Assess the morphology of the erythrocytes.
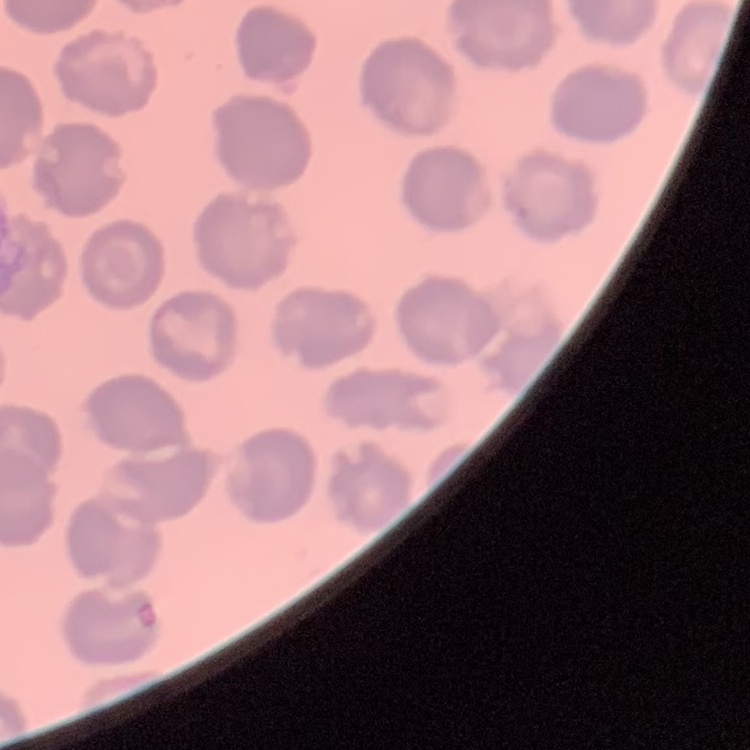
No rouleaux formation.

Summary:
  - Image type: one tile cut from a larger photomicrograph
  - Stain: Field's or Giemsa
  - Preparation: thin peripheral smear